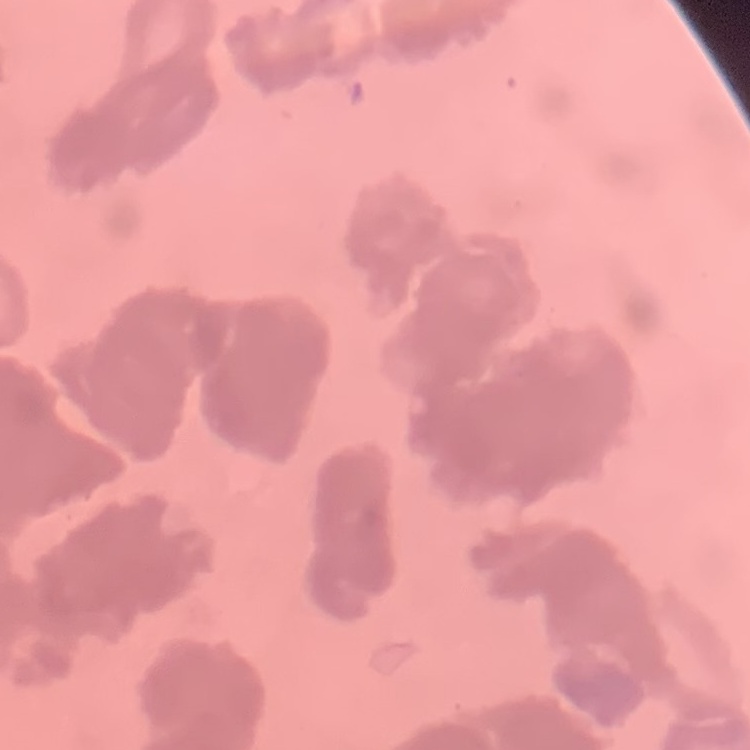

Summary:
  - Erythrocyte morphology: rouleaux formation
  - Image type: one tile cut from a larger photomicrograph
  - Preparation: thin blood smear
  - Stain: Field's or Giemsa